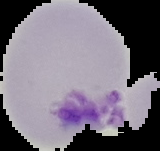
{
  "image_size": "160×151 pixels",
  "preparation": "thin blood film",
  "image_type": "segmented cell region with the area outside set to black",
  "malaria_status": "uninfected"
}